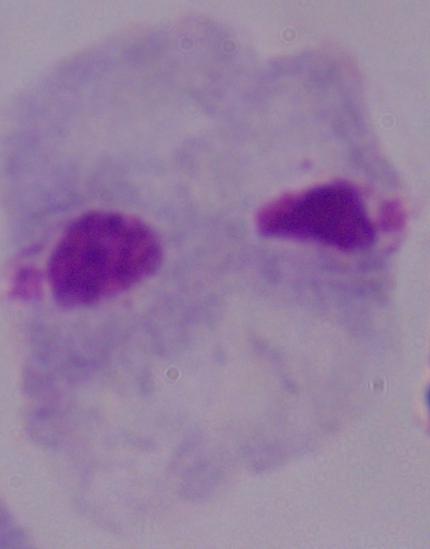
Summary:
  - Modality: micrograph
  - Magnification: 1000x
  - Identification: trichomonad